Assess this cell for malaria.
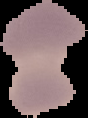

It is parasitized.

Image is 88×118 pixels. From a thin blood smear. The area outside the segmented cell region is set to black.